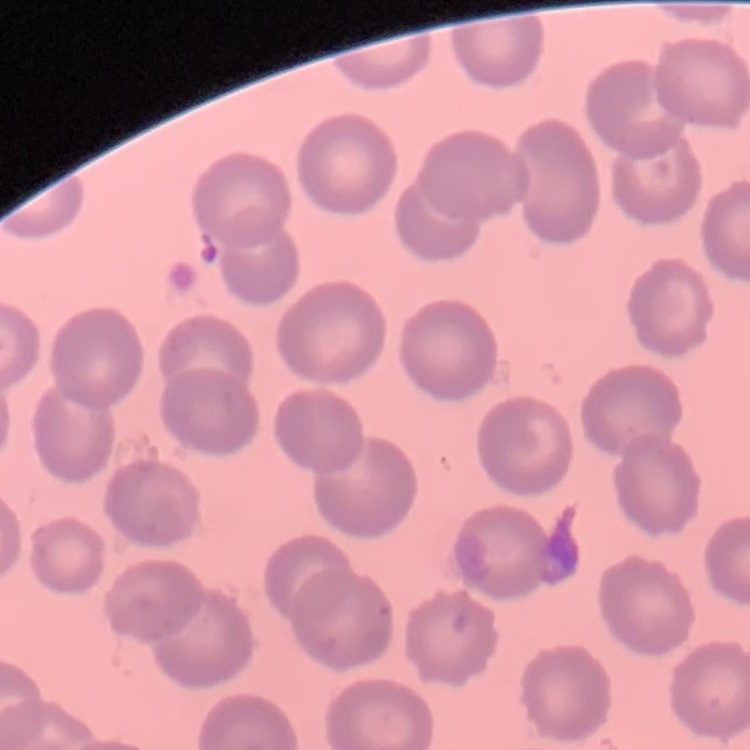
red_blood_cell_morphology: no rouleaux formation
stain: Field's or Giemsa
preparation: thin blood film
image_type: square crop of a larger photomicrograph